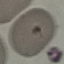
Summary:
  - Malaria status: parasitized
  - Preparation: thin smear
  - Stain: Giemsa
  - Capture: smartphone through the microscope eyepiece
  - Image type: cell patch, automatically extracted from a larger field of view and resized to 64 × 64 pixels